Describe the morphology of the erythrocytes.
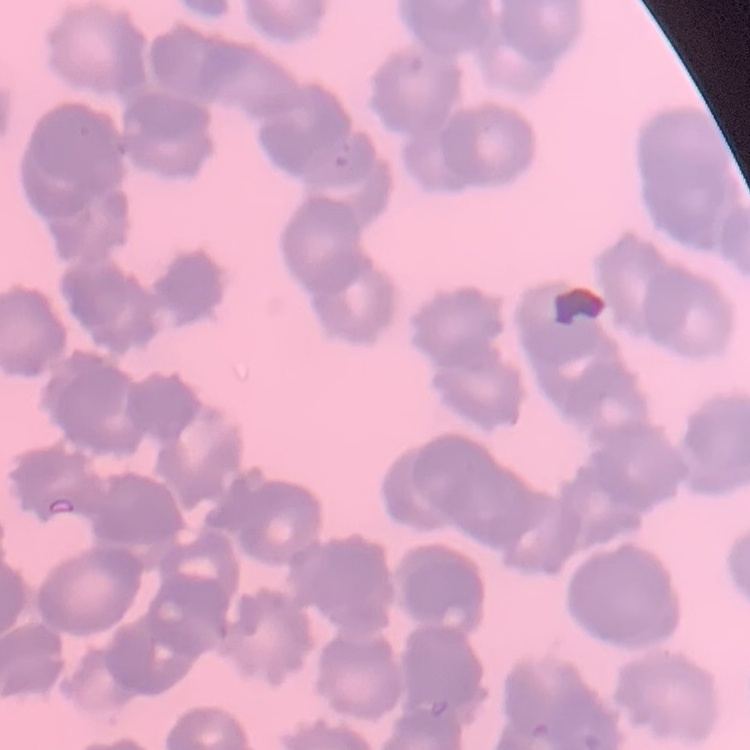

Rouleaux formation.

Thin peripheral smear. Stained with either Field's or Giemsa. One tile cut from a larger photomicrograph.